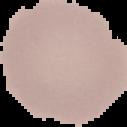 Cell region segmented out of the field of view; the surrounding area is masked to black. From a thin blood smear. Image is 127×127 pixels. Result: no malaria parasites seen.